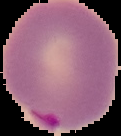
Malaria status: parasitized. Cell region segmented out of the field of view; the surrounding area is masked to black. Image is 121×136 pixels. From a thin blood smear.